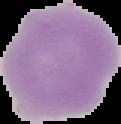
From a thin blood smear. Cell region segmented out of the field of view; the surrounding area is masked to black. Result: no Plasmodium parasites seen. Image is 121×124 pixels.